Give the position of every Plasmodium parasite visible.
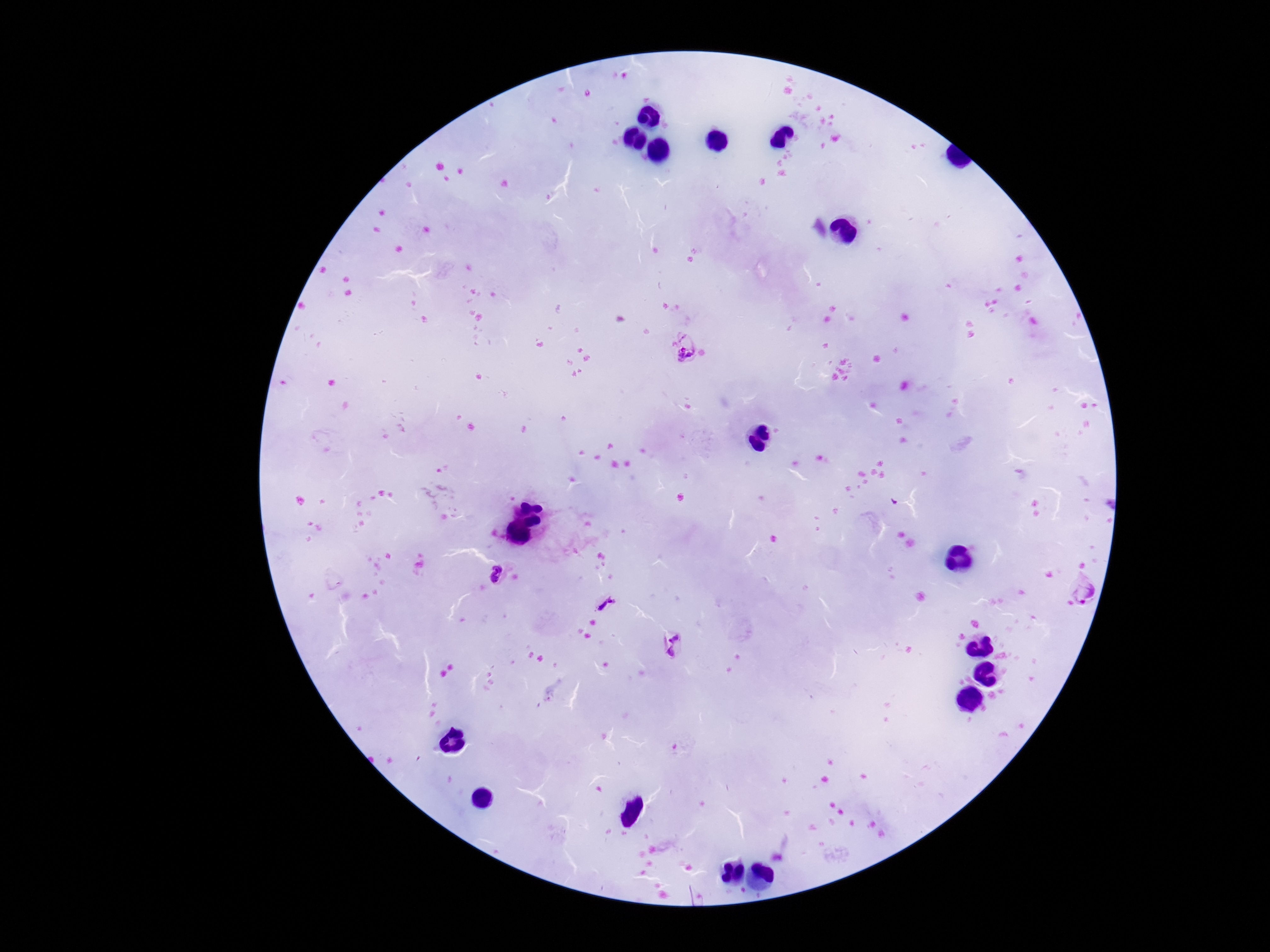

Approximate centers as [x, y] in pixels.
Plasmodium parasites: [684, 347], [497, 573], [1082, 589], [604, 603], [673, 646].

magnification = 100x
image size = 1270×952 pixels
field of view = one from this slide
stain = Giemsa
patient malaria status = infected
capture = smartphone camera through the microscope eyepiece
preparation = thick blood film